Report the malaria status of this cell.
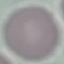

It is uninfected.

{
  "stain": "Giemsa",
  "capture": "smartphone through the microscope eyepiece",
  "preparation": "thin smear",
  "image_type": "automatically extracted cell patch, resized to 64 × 64 pixels"
}